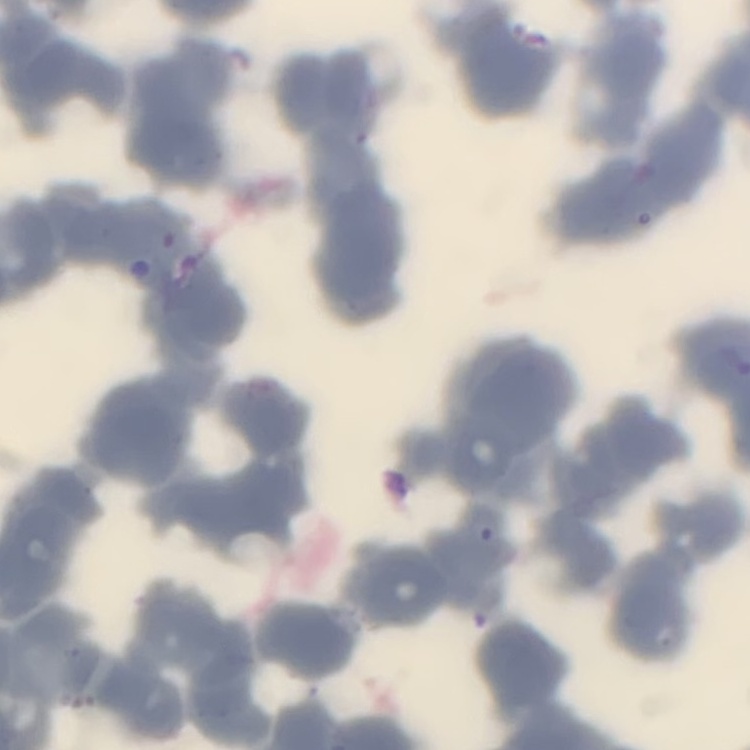
{
  "red_blood_cell_morphology": "rouleaux formation",
  "stain": "Field's or Giemsa",
  "image_type": "one tile cut from a larger photomicrograph",
  "preparation": "thin blood film"
}